Name the blood parasite species.
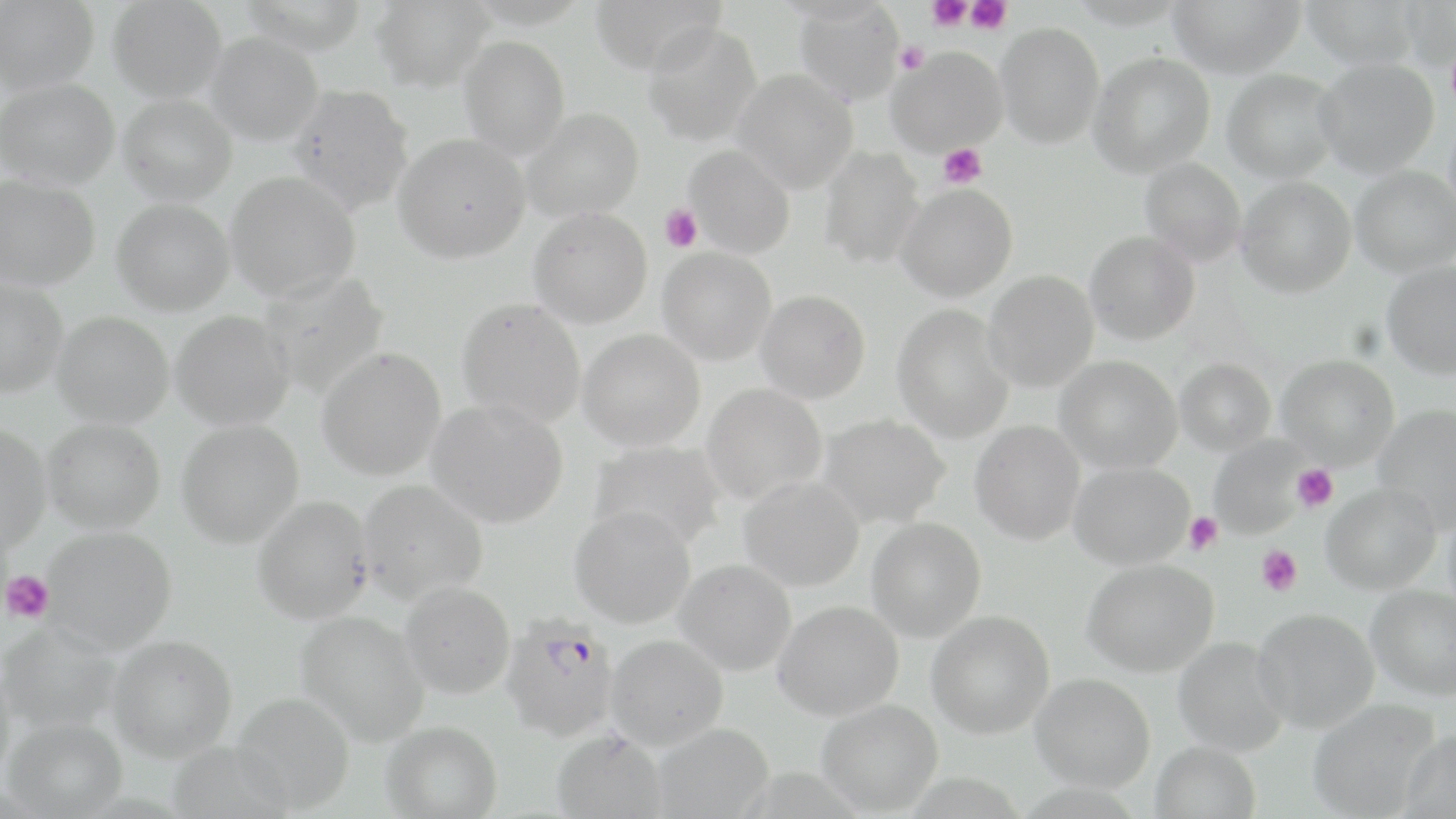
Plasmodium falciparum.

stain = May-Grünwald-Giemsa
uninfected red blood cell locations = approximate bounding boxes as [x1, y1, x2, y2] in pixels: [0, 0, 99, 94], [107, 0, 227, 102], [239, 0, 369, 55], [371, 0, 493, 92], [590, 0, 726, 76], [1068, 0, 1188, 29], [1168, 0, 1305, 78], [1301, 0, 1419, 71], [1400, 1, 1456, 72], [792, 2, 904, 104], [642, 22, 761, 147], [995, 22, 1104, 149], [205, 32, 323, 146], [459, 36, 570, 160], [886, 47, 1007, 157], [1089, 53, 1215, 177], [1314, 59, 1439, 178], [1222, 69, 1340, 183], [733, 70, 859, 193], [1, 77, 119, 190], [288, 84, 414, 215], [118, 94, 237, 205], [520, 107, 644, 222], [393, 132, 530, 263], [683, 145, 795, 258], [817, 147, 924, 269], [1139, 158, 1247, 265], [1351, 166, 1456, 277], [225, 171, 360, 302], [0, 174, 100, 291], [1235, 176, 1356, 298], [896, 183, 1018, 302], [111, 198, 234, 316], [528, 207, 653, 329], [1084, 232, 1200, 345], [657, 246, 778, 366], [1382, 261, 1456, 379], [984, 271, 1099, 393], [259, 272, 389, 398], [0, 277, 68, 398], [755, 290, 870, 404], [456, 296, 587, 428], [893, 304, 1014, 444], [171, 310, 294, 431], [52, 312, 174, 428], [578, 329, 705, 451], [316, 347, 447, 480], [1276, 354, 1399, 469], [1055, 356, 1182, 474], [1175, 358, 1275, 456], [701, 384, 827, 504], [426, 399, 569, 528], [1373, 404, 1456, 531], [818, 414, 950, 529], [42, 419, 166, 533], [176, 420, 304, 548], [970, 420, 1085, 545], [0, 424, 51, 555], [1209, 436, 1309, 540], [589, 441, 727, 551], [1068, 462, 1194, 570], [738, 475, 865, 591], [357, 479, 488, 604], [1321, 483, 1441, 594], [252, 495, 374, 624], [569, 505, 696, 628], [1443, 505, 1456, 621], [866, 518, 986, 642], [41, 526, 177, 654], [674, 559, 796, 675], [1082, 559, 1218, 677], [400, 581, 516, 699], [1365, 585, 1456, 701], [773, 600, 903, 721], [1252, 609, 1379, 733], [295, 610, 430, 745], [926, 611, 1054, 739], [1, 623, 121, 735], [107, 634, 237, 762], [607, 635, 728, 749], [1173, 637, 1288, 757], [0, 661, 16, 790], [1030, 673, 1155, 792], [233, 692, 355, 813], [1308, 699, 1438, 819], [817, 700, 943, 815], [4, 717, 127, 817], [382, 720, 502, 818], [653, 723, 774, 818], [551, 728, 668, 819], [1397, 729, 1456, 819], [168, 741, 291, 817], [1150, 742, 1261, 819]
preparation = thin blood smear
platelet locations = approximate bounding boxes as [x1, y1, x2, y2] in pixels: [927, 0, 971, 30], [966, 0, 1012, 34], [895, 41, 929, 74], [939, 143, 986, 189], [659, 204, 703, 252], [1292, 464, 1338, 511], [1184, 512, 1223, 554], [1256, 546, 1302, 595], [2, 570, 53, 623]
modality = light microscopy
field of view = one of a larger specimen
Plasmodium falciparum-infected red blood cell locations = approximate bounding boxes as [x1, y1, x2, y2] in pixels: [500, 615, 620, 740]
magnification = 1000x
image size = 1456×819 pixels